Classify this cell by malaria status.
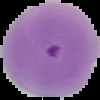
Parasitized.

image type = segmented cell region with the area outside set to black
preparation = thin blood smear
image size = 100×100 pixels